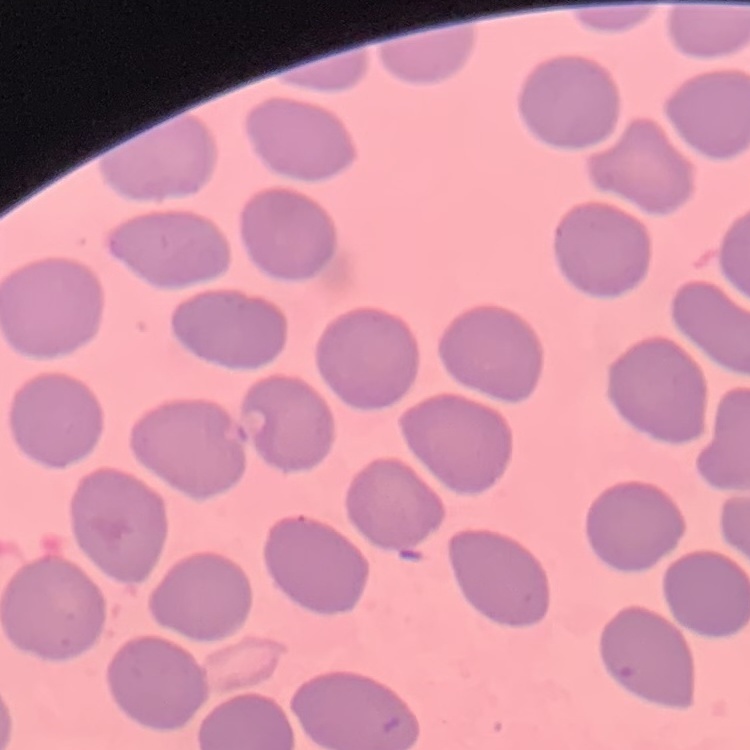

erythrocyte morphology = no rouleaux formation
preparation = thin peripheral smear
stain = Field's or Giemsa
image type = square crop of a larger photomicrograph